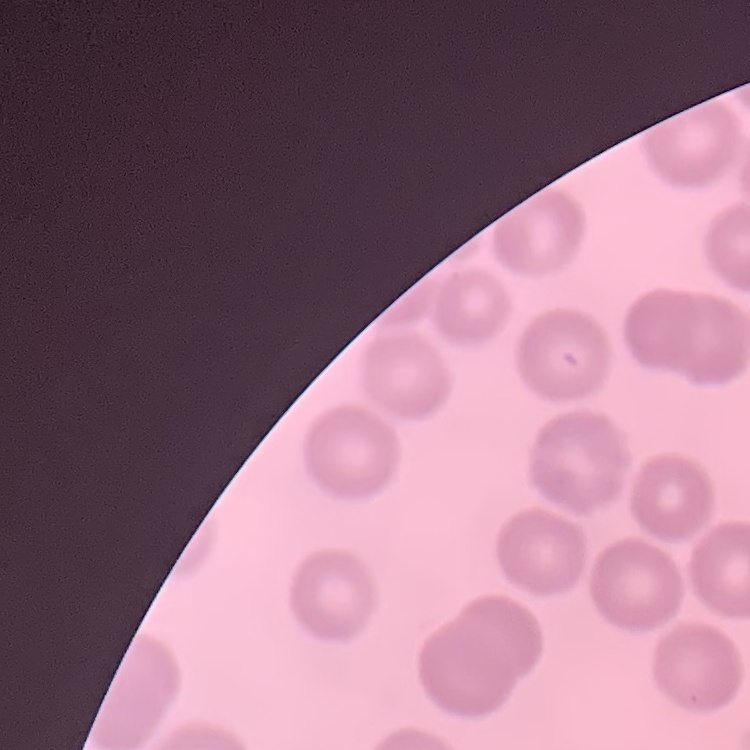
The erythrocytes show no rouleaux formation. One tile cut from a larger photomicrograph. Thin blood film. Stained with either Field's or Giemsa.